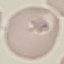
Summary:
  - Malaria status: uninfected
  - Capture: smartphone through the microscope eyepiece
  - Stain: Giemsa
  - Image type: automatically extracted cell patch, resized to 64 × 64 pixels
  - Preparation: thin blood film